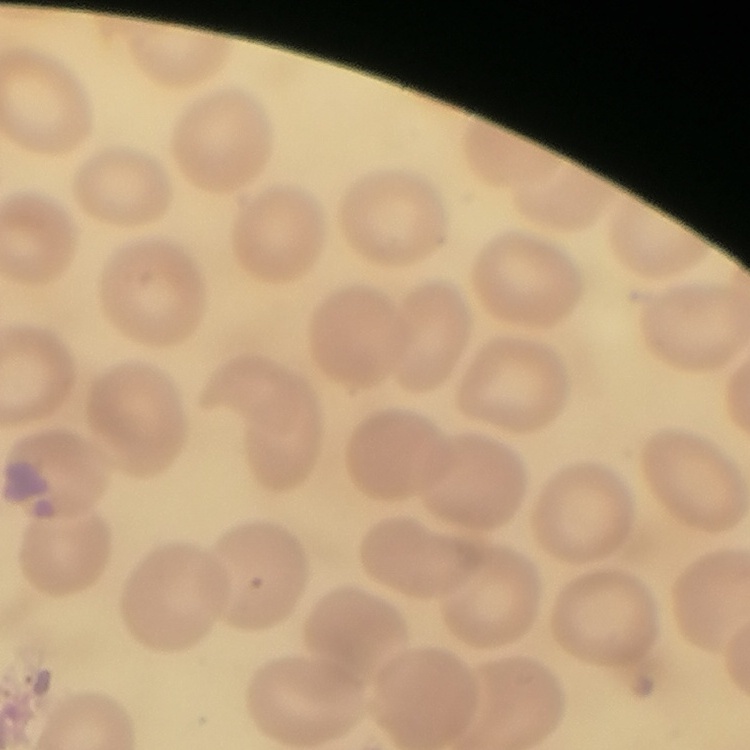
Summary:
  - Erythrocyte morphology: no rouleaux formation
  - Preparation: thin blood film
  - Stain: Field's or Giemsa
  - Image type: square crop of a larger photomicrograph